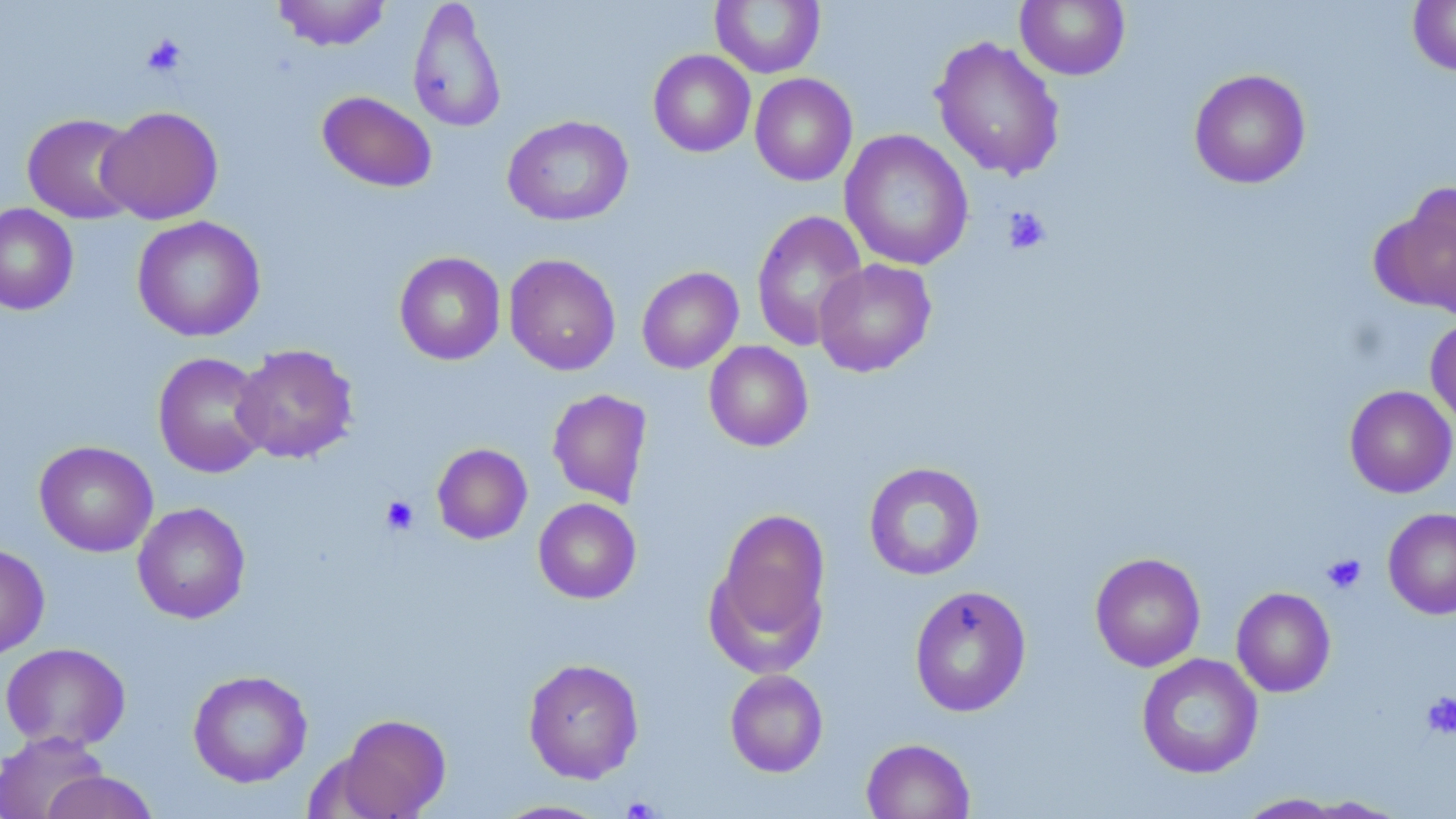

Summary:
  - Coordinate format: approximate bounding boxes as (x1,y1)-(x2,y2) corner pairs in pixels
  - Uninfected red blood cell locations: (273,0)-(392,51), (407,0)-(507,134), (1015,0)-(1130,80), (1408,0)-(1456,76), (710,1)-(826,78), (930,35)-(1066,181), (648,50)-(756,157), (1189,68)-(1311,189), (749,73)-(857,186), (316,90)-(438,193), (99,106)-(223,224), (22,113)-(142,224), (502,115)-(633,226), (839,129)-(974,271), (1379,183)-(1456,316), (0,203)-(79,316), (751,210)-(868,351), (132,215)-(265,342), (394,251)-(506,365), (504,253)-(621,376), (814,259)-(937,377), (637,267)-(743,373), (1425,316)-(1456,432), (703,341)-(813,452), (231,344)-(359,464), (152,351)-(272,478), (1344,385)-(1456,498), (547,388)-(653,508), (34,441)-(158,557), (432,443)-(532,544), (863,462)-(985,581), (533,498)-(641,604), (132,503)-(251,624), (710,507)-(831,664), (1383,508)-(1456,619), (0,544)-(49,660), (1090,552)-(1206,672), (910,584)-(1032,716), (1231,587)-(1336,697), (1,642)-(131,752), (1136,653)-(1263,779), (523,658)-(643,783), (187,669)-(313,788), (725,669)-(828,777), (336,713)-(451,818), (0,731)-(109,819), (861,738)-(974,818), (39,771)-(161,819), (1235,793)-(1350,818), (1295,795)-(1411,817), (491,799)-(614,818)
  - Platelet locations: (141,34)-(187,78), (1003,206)-(1052,255), (380,495)-(420,535), (1321,553)-(1367,594), (1420,691)-(1456,739), (621,796)-(661,819)
  - Slide-level diagnosis: no evidence of blood parasites
  - Image size: 1456×819 pixels
  - Stain: May-Grünwald-Giemsa
  - Preparation: thin blood film
  - Modality: optical microscopy
  - Magnification: 1000x
  - Field of view: one of a larger specimen